Point out each malaria parasite.
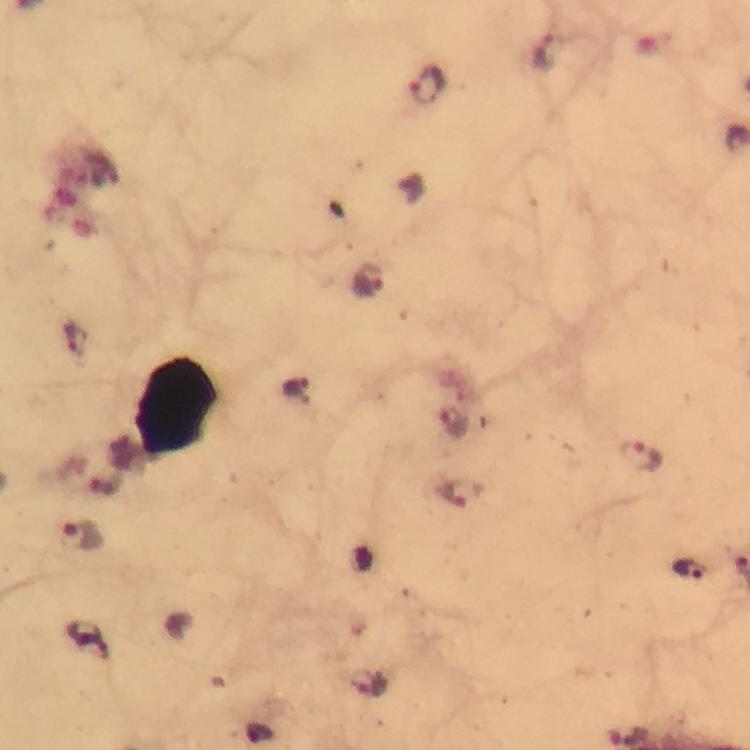
Approximate centers as [x, y] in pixels.
Malaria parasites: [546, 53], [428, 86], [369, 281], [75, 340], [295, 389], [454, 422], [643, 457], [461, 492], [83, 536], [688, 570], [368, 685].

Summary:
  - Image size: 750×750 pixels
  - Cropped from: a single field of view
  - Preparation: thick blood smear
  - Capture: smartphone mounted on the microscope
  - Stain: Giemsa
  - Context: from a diagnostic examination for malaria
  - Magnification: 100x
  - Immersion oil: used